Classify this cell by malaria status.
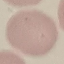

It is uninfected.

Summary:
  - Preparation: thin blood smear
  - Capture: smartphone camera at the microscope eyepiece
  - Stain: Giemsa
  - Image type: automatically extracted cell patch, resized to 64 × 64 pixels